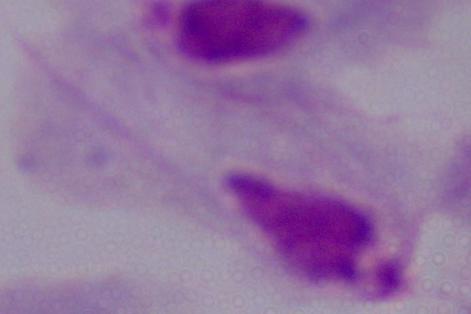

Summary:
  - Magnification: 1000x
  - Modality: micrograph
  - Identification: trichomonad